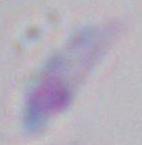

Micrograph. Toxoplasma gondii is shown. Captured at 1000x magnification.